Locate every Plasmodium parasite and every leukocyte.
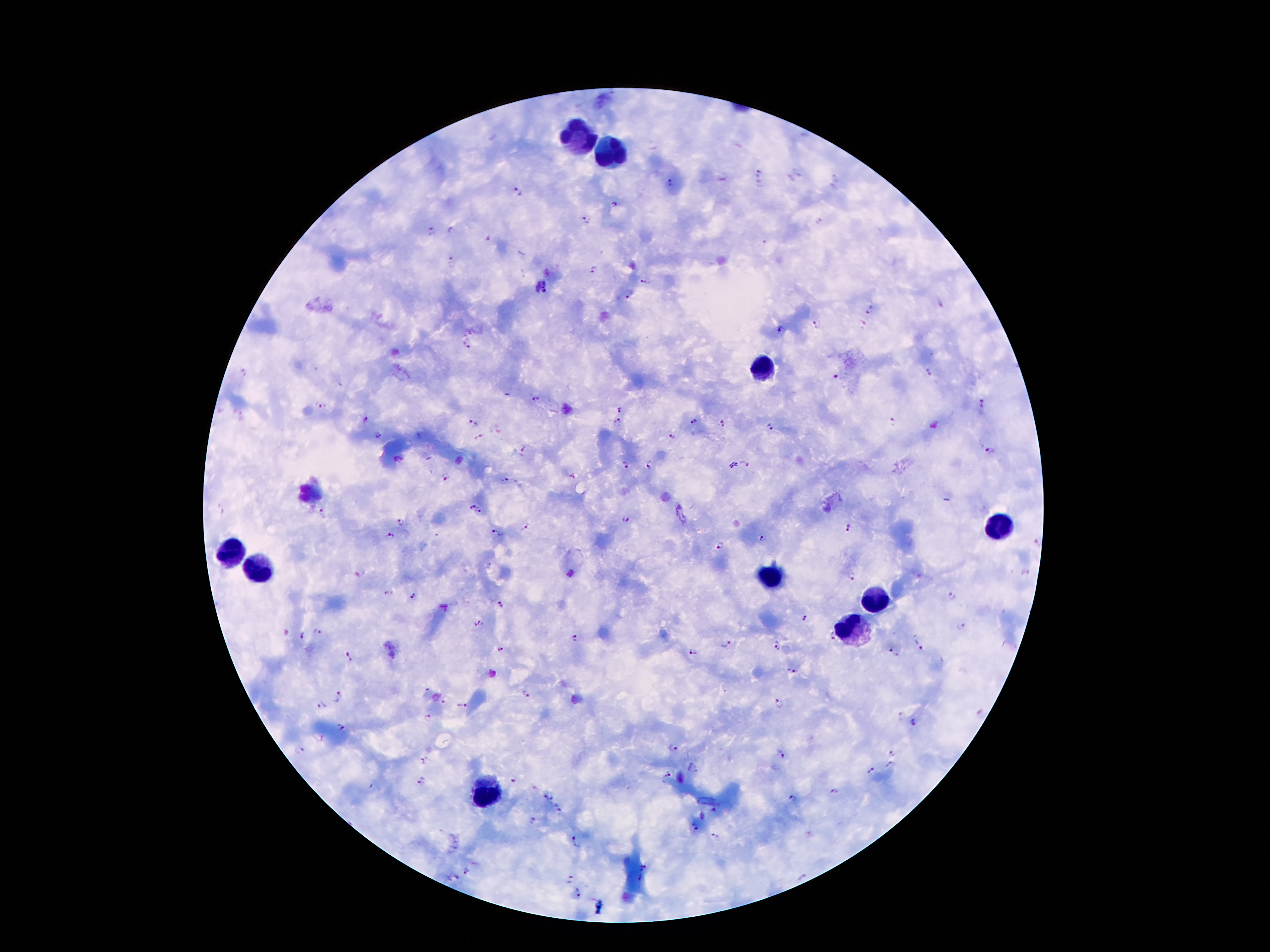

Approximate centers as (x, y) in pixels.
Plasmodium parasites: (759, 172), (670, 183), (517, 192), (614, 203), (586, 220), (452, 228), (430, 231), (487, 241), (449, 259), (593, 271), (646, 280), (542, 285), (628, 298), (871, 310), (817, 324), (470, 329), (782, 331), (464, 344), (930, 372), (243, 374), (836, 376), (536, 400), (984, 404), (322, 406), (620, 408), (366, 419), (692, 421), (473, 423), (617, 423), (721, 423), (893, 423), (933, 424), (769, 428), (495, 429), (377, 435), (670, 436), (480, 439), (523, 447), (991, 451), (650, 463), (744, 464), (625, 465), (571, 477), (444, 478), (503, 479), (472, 507), (480, 511), (322, 514), (624, 518), (401, 520), (524, 528), (847, 528), (498, 534), (389, 535), (763, 538), (718, 545), (360, 570), (1025, 574), (853, 576), (389, 593), (413, 596), (954, 596), (502, 603), (805, 619), (479, 623), (961, 628), (319, 631), (304, 635), (573, 638), (726, 646), (775, 648), (918, 648), (501, 650), (893, 652), (692, 653), (349, 657), (792, 670), (425, 689), (525, 695), (340, 697), (778, 703), (321, 706), (460, 706), (899, 716), (425, 718), (914, 724), (341, 727), (673, 747), (299, 751), (893, 751), (780, 756), (425, 760), (891, 766), (692, 767), (870, 770), (667, 774), (513, 780), (422, 781), (834, 792), (548, 798), (792, 799), (558, 810), (533, 819), (692, 828), (714, 837), (575, 842), (466, 872), (569, 879), (577, 894).
Leukocytes: (582, 136), (605, 151), (762, 368), (1002, 525), (230, 549), (254, 569), (773, 574), (875, 600), (854, 630), (491, 791).

Summary:
  - Stain: Giemsa
  - Field of view: single
  - Magnification: 100x
  - Capture: smartphone camera through the microscope eyepiece
  - Patient malaria status: infected with Plasmodium falciparum
  - Preparation: thick blood film
  - Image size: 1270×952 pixels